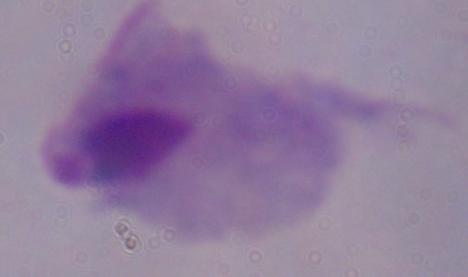
identification = trichomonad
modality = micrograph
magnification = 1000x